Outline each Plasmodium falciparum-infected red blood cell.
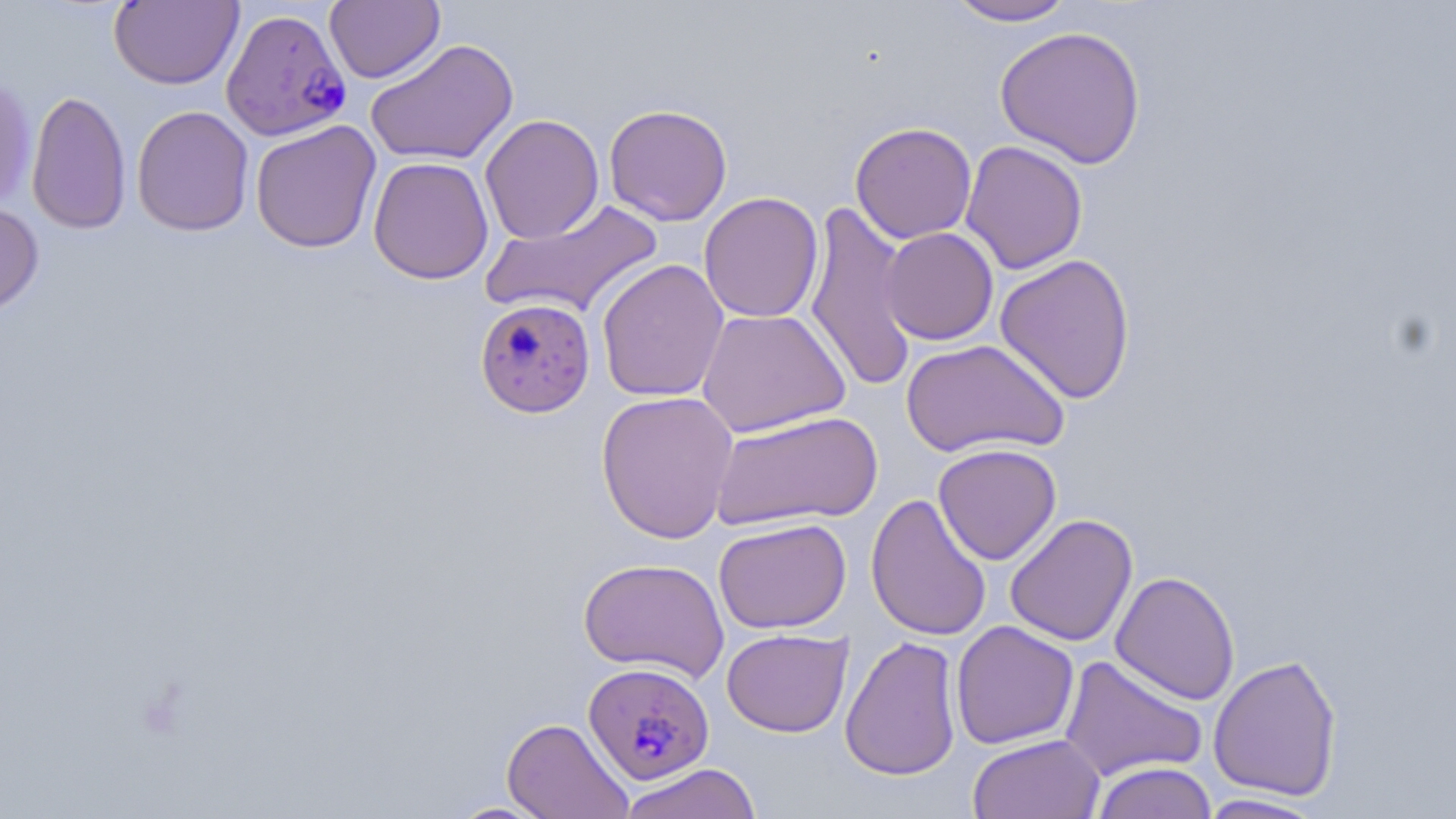

Approximate bounding boxes as (x1,y1)-(x2,y2) corner pairs in pixels.
Plasmodium falciparum-infected red blood cells: (220,7)-(352,142), (473,297)-(596,418), (583,662)-(714,786).

Uninfected red blood cell locations: (944,0)-(1078,27), (108,1)-(244,90), (325,1)-(445,84), (994,25)-(1147,168), (365,38)-(519,166), (0,72)-(36,211), (26,89)-(132,235), (603,104)-(733,226), (132,106)-(254,236), (479,114)-(605,244), (250,120)-(382,253), (850,122)-(978,244), (960,140)-(1088,274), (368,157)-(494,285), (698,192)-(824,323), (804,198)-(918,396), (480,199)-(665,321), (0,202)-(45,318), (881,227)-(998,345), (995,253)-(1136,404), (595,258)-(730,402), (696,308)-(851,438), (901,338)-(1071,460), (595,390)-(740,544), (709,409)-(882,531), (932,443)-(1062,565), (865,493)-(992,642), (1004,513)-(1138,647), (713,518)-(852,634), (578,557)-(729,681), (1110,571)-(1241,705), (950,620)-(1079,750), (721,628)-(853,737), (840,635)-(962,781), (1059,654)-(1208,782), (1208,654)-(1342,801), (502,717)-(633,818), (967,733)-(1105,819), (1090,761)-(1217,819), (617,762)-(762,819), (1194,793)-(1329,818), (447,800)-(555,818). Slide-level diagnosis: Plasmodium falciparum. Captured at 1000x magnification. Optical microscopy. Thin blood film. One field of a larger specimen. May-Grünwald-Giemsa stain. Image is 1456×819 pixels.